Comment on the morphology of the erythrocytes.
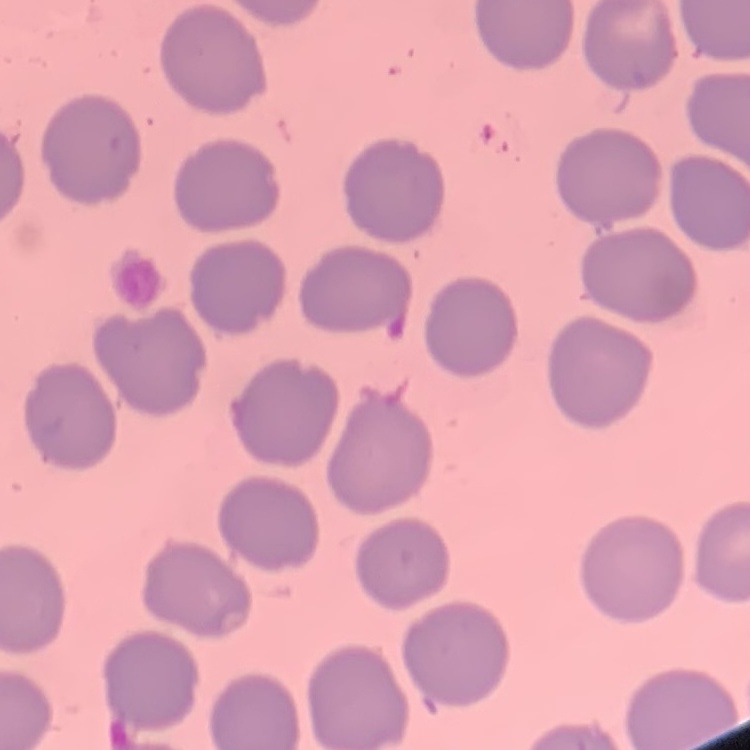
No rouleaux formation.

Summary:
  - Preparation: thin blood film
  - Image type: square crop of a larger photomicrograph
  - Stain: Field's or Giemsa